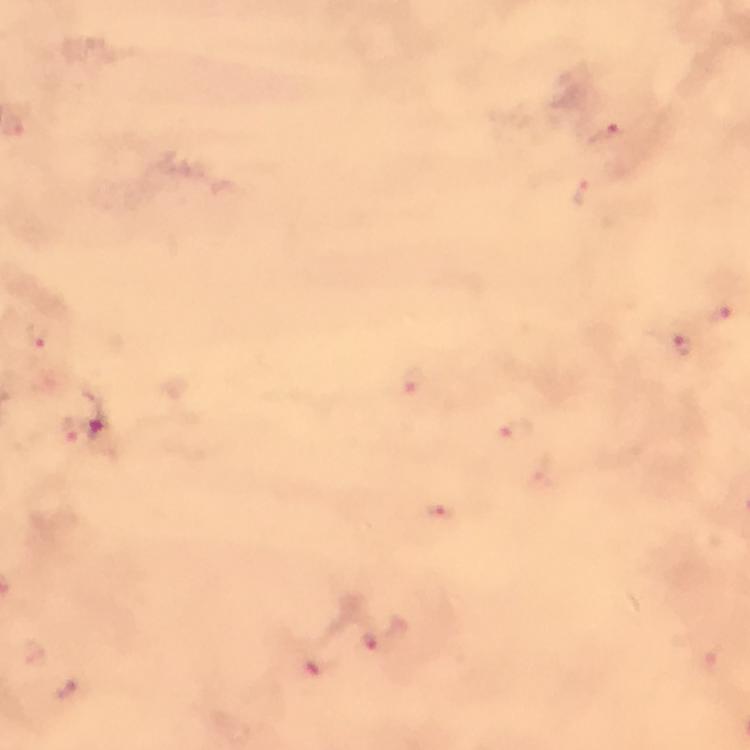

Approximate centers as [x, y] in pixels.
Summary:
  - Malaria parasite locations: [603, 135], [581, 193], [720, 314], [40, 335], [683, 347], [411, 380], [69, 427], [517, 428], [544, 474], [441, 514], [369, 637], [314, 662], [70, 692]
  - Stain: Giemsa
  - Capture: smartphone mounted on the microscope
  - Context: from a diagnostic examination for malaria
  - Preparation: thick smear
  - Immersion oil: applied
  - Image size: 750×750 pixels
  - Magnification: 100x
  - Cropped from: one field of view